Classify this cell by malaria status.
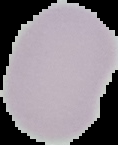

It is uninfected.

Summary:
  - Image size: 118×145 pixels
  - Preparation: thin blood smear
  - Image type: cell region segmented out of the field of view; surrounding area masked to black